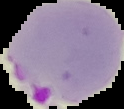

Summary:
  - Image type: segmented cell region with the area outside set to black
  - Result: malaria parasites detected
  - Image size: 124×109 pixels
  - Preparation: thin blood film